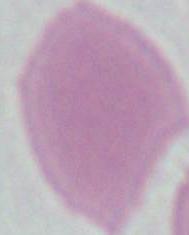
Captured at 1000x magnification. Photomicrograph. A red blood cell is seen.